Give the extent of all Plasmodium falciparum-infected red blood cells.
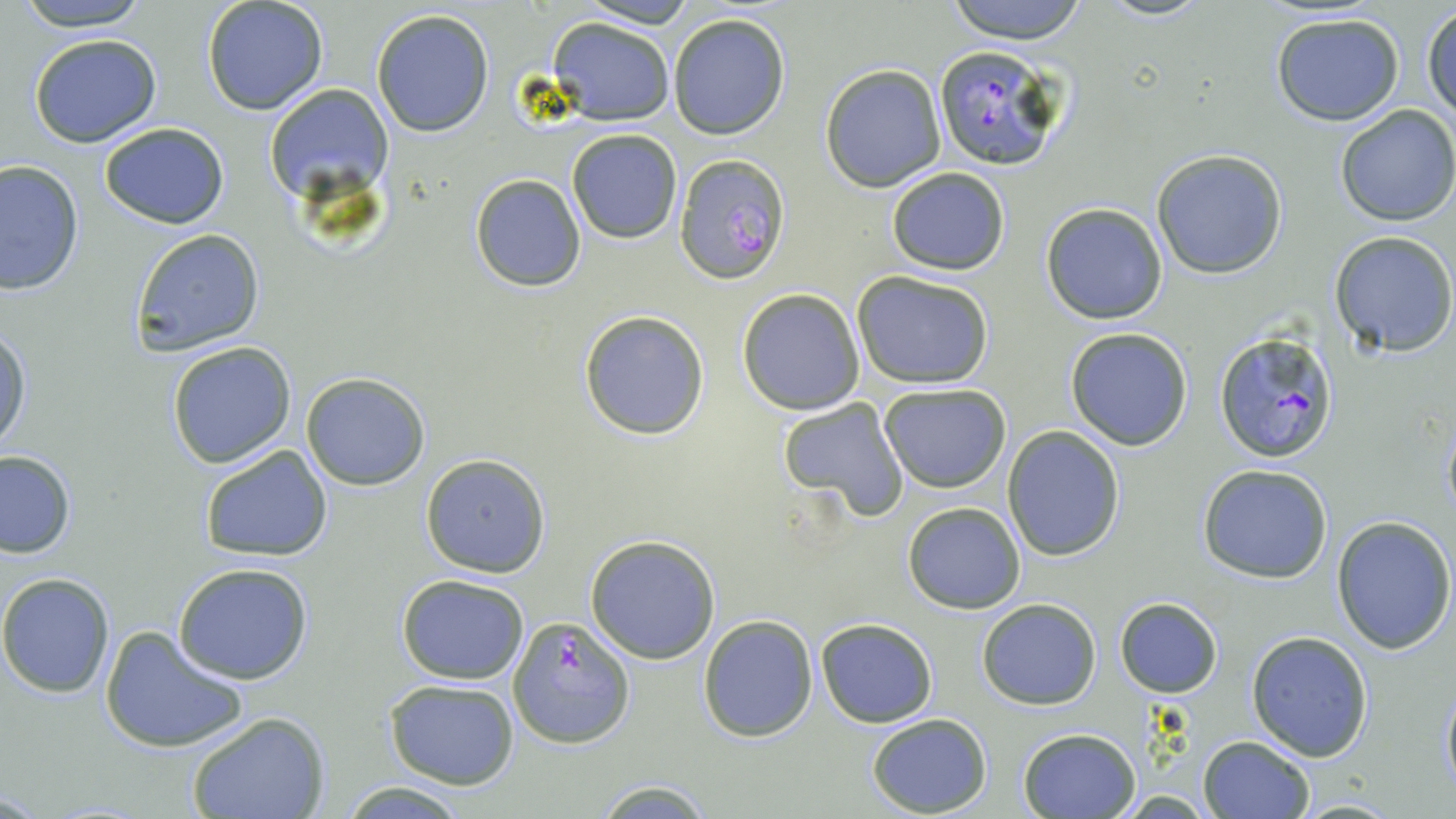

Approximate bounding boxes as (x1,y1)-(x2,y2) corner pairs in pixels.
Plasmodium falciparum-infected red blood cells: (931,44)-(1067,171), (673,154)-(791,285), (1215,330)-(1340,464), (509,616)-(631,748).

Uninfected red blood cell locations: (12,0)-(154,32), (201,0)-(330,116), (575,0)-(699,28), (943,0)-(1092,43), (1096,0)-(1214,22), (1423,6)-(1455,126), (370,8)-(494,138), (1269,12)-(1405,126), (666,13)-(791,139), (547,18)-(674,126), (28,34)-(162,148), (820,63)-(946,192), (265,82)-(393,198), (1334,103)-(1456,226), (98,122)-(229,230), (566,128)-(683,244), (1152,149)-(1288,279), (0,159)-(84,298), (885,167)-(1011,276), (469,173)-(588,292), (1039,202)-(1168,324), (129,229)-(265,356), (1328,230)-(1456,357), (852,271)-(995,388), (736,288)-(865,415), (578,309)-(710,441), (0,324)-(32,455), (1064,327)-(1194,451), (165,341)-(296,468), (301,372)-(431,491), (878,382)-(1012,494), (776,397)-(910,523), (1440,408)-(1456,525), (1002,424)-(1125,561), (198,444)-(335,564), (0,450)-(76,558), (419,454)-(552,577), (1197,464)-(1334,583), (903,500)-(1025,612), (1331,515)-(1455,654), (585,533)-(722,664), (173,562)-(314,685), (0,571)-(117,696), (395,573)-(529,684), (1115,597)-(1222,698), (977,600)-(1102,710), (698,615)-(818,740), (815,618)-(938,728), (100,627)-(249,754), (1245,630)-(1374,760), (385,679)-(520,789), (1439,680)-(1456,796), (186,711)-(330,819), (867,714)-(993,817), (1017,728)-(1139,818), (1198,734)-(1314,818), (591,777)-(716,817), (1292,797)-(1405,817). Slide-level diagnosis: Plasmodium falciparum. Image is 1456×819 pixels. May-Grünwald-Giemsa-stained preparation. Optical microscopy. 1000x magnification. One field of a larger specimen. Thin blood film.